State which parasite is depicted.
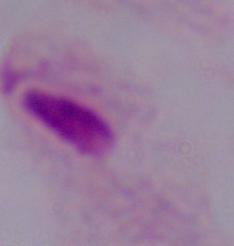
This is a trichomonad.

magnification = 1000x
modality = micrograph